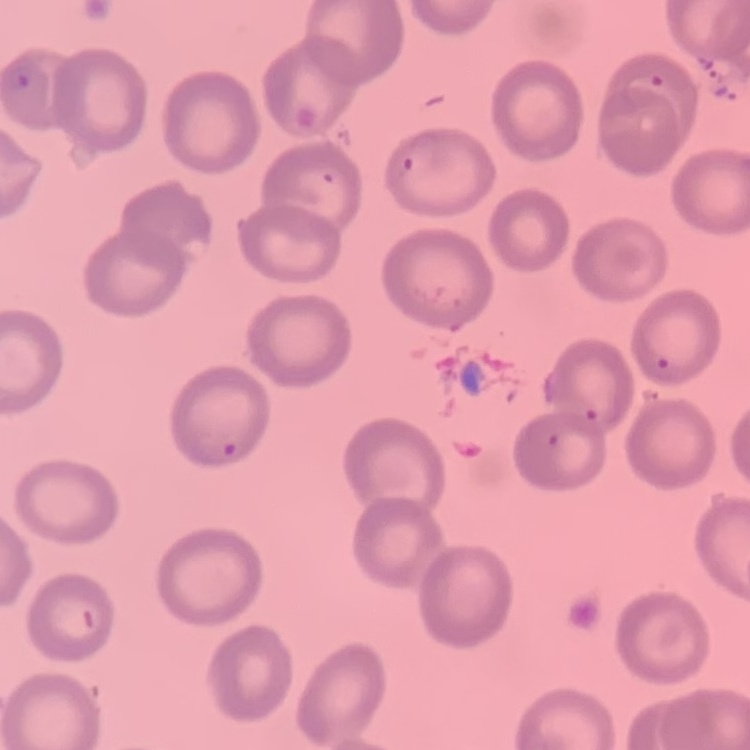

Summary:
  - Erythrocyte morphology: no rouleaux formation
  - Stain: Field's or Giemsa
  - Image type: square crop of a larger photomicrograph
  - Preparation: thin blood smear